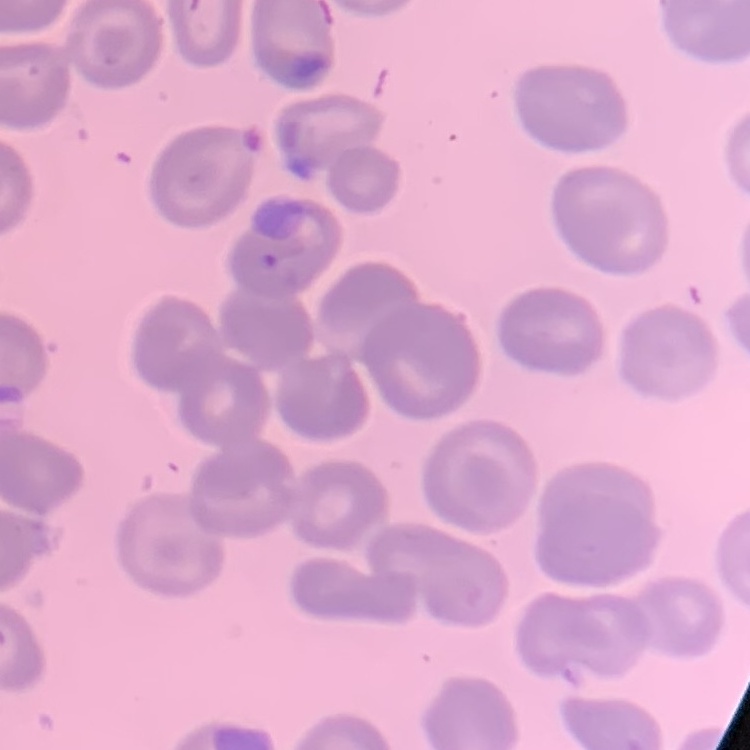
The erythrocytes exhibit no rouleaux formation. Thin blood smear. Square crop of a larger photomicrograph. Field's or Giemsa stain.